Look for Plasmodium parasites.
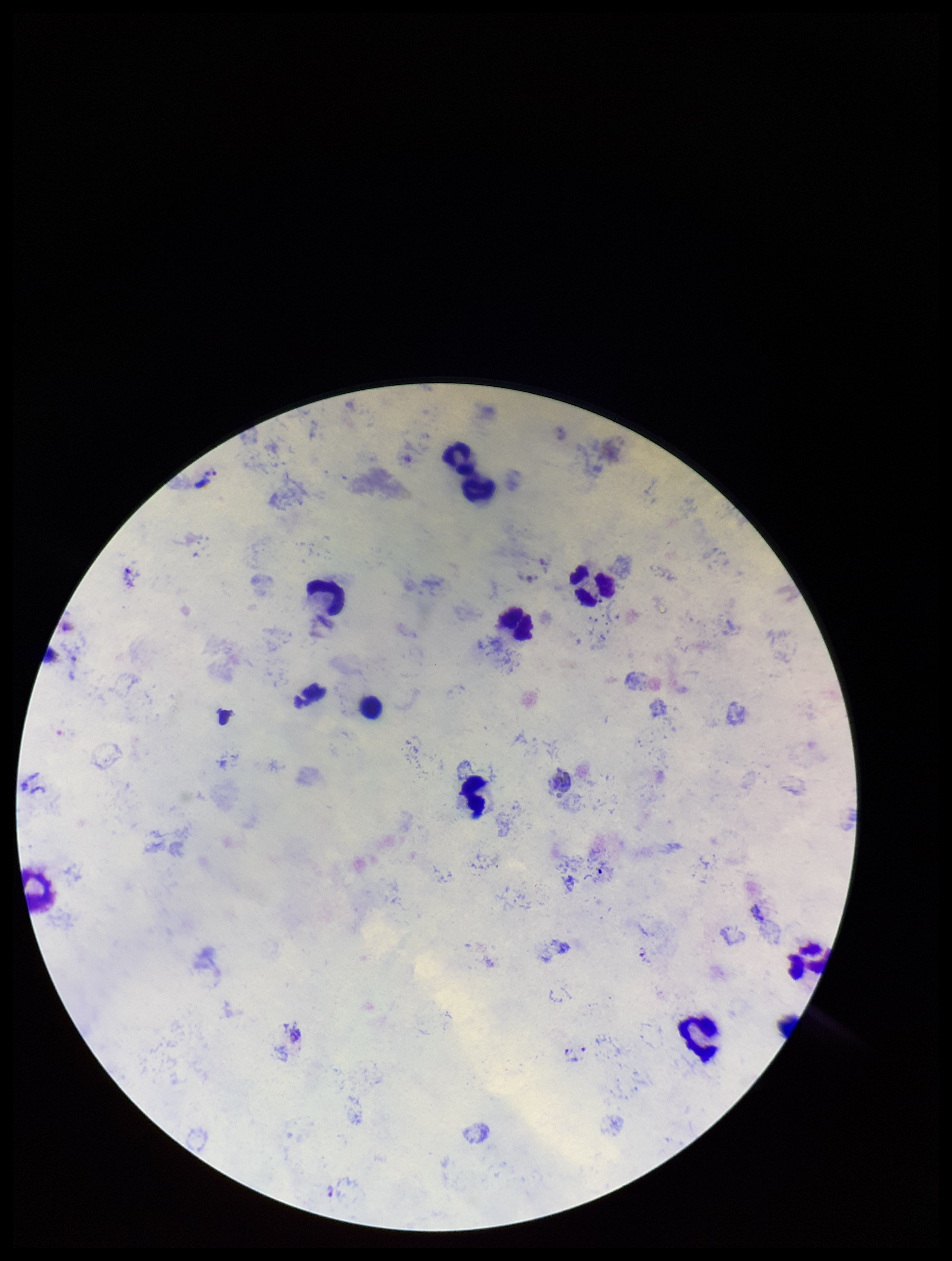
Identified.

Summary:
  - Preparation: thick smear
  - Parasite count: 5
  - Patient malaria status: infected
  - Image size: 952×1261 pixels
  - Capture: smartphone photograph through the microscope eyepiece
  - Leukocyte count: 10
  - Field of view: single
  - Stain: Giemsa
  - Species reported for this patient: Plasmodium vivax